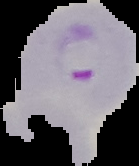
preparation: thin blood smear
image_size: 139×166 pixels
image_type: cell region segmented out of the field of view; surrounding area masked to black
malaria_status: parasitized